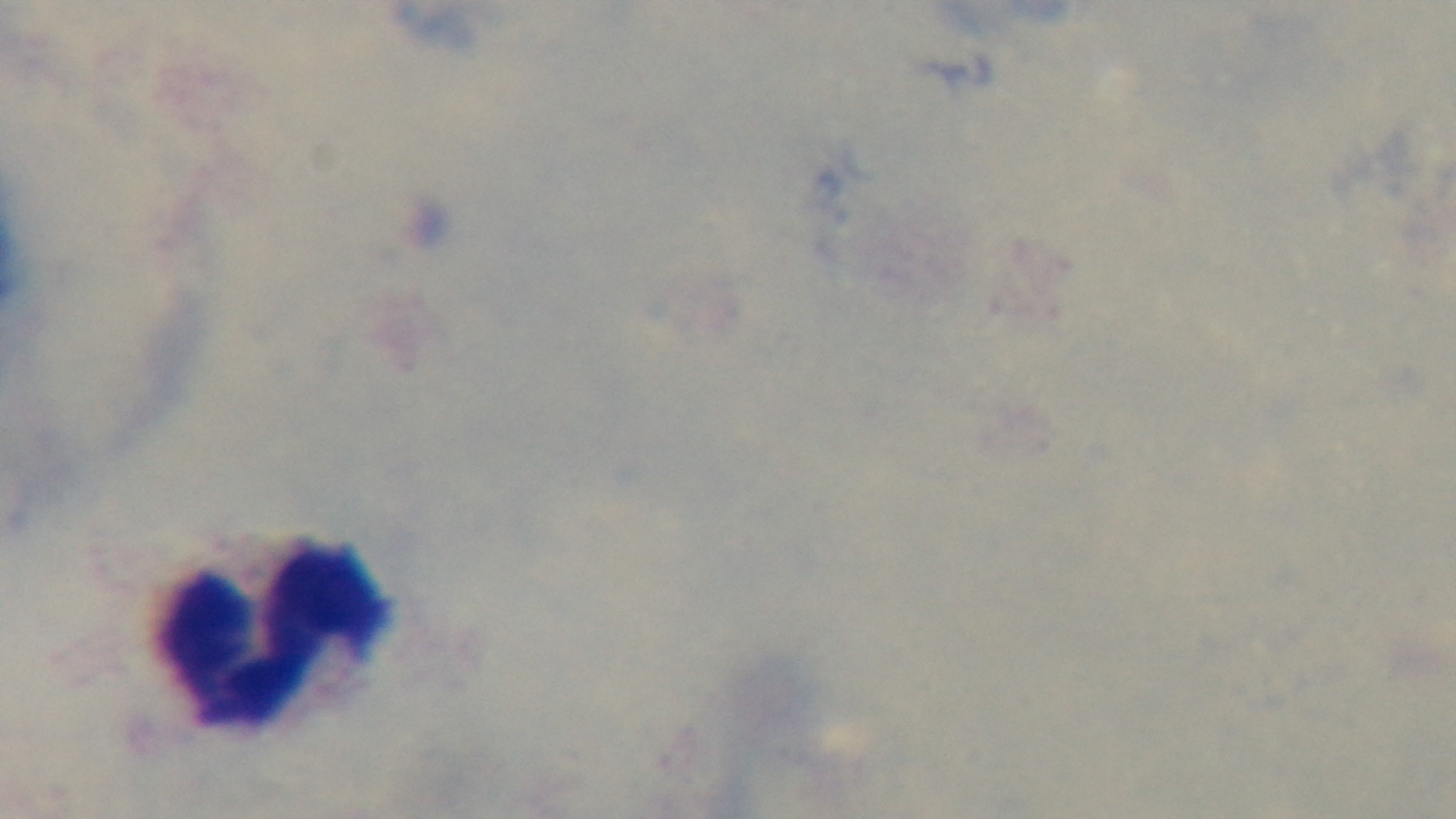

capture: mounted 4K digital camera
stain: Giemsa
malaria_status: negative
modality: light microscopy
preparation: thick blood film
field_of_view: single
objective: 100x oil immersion